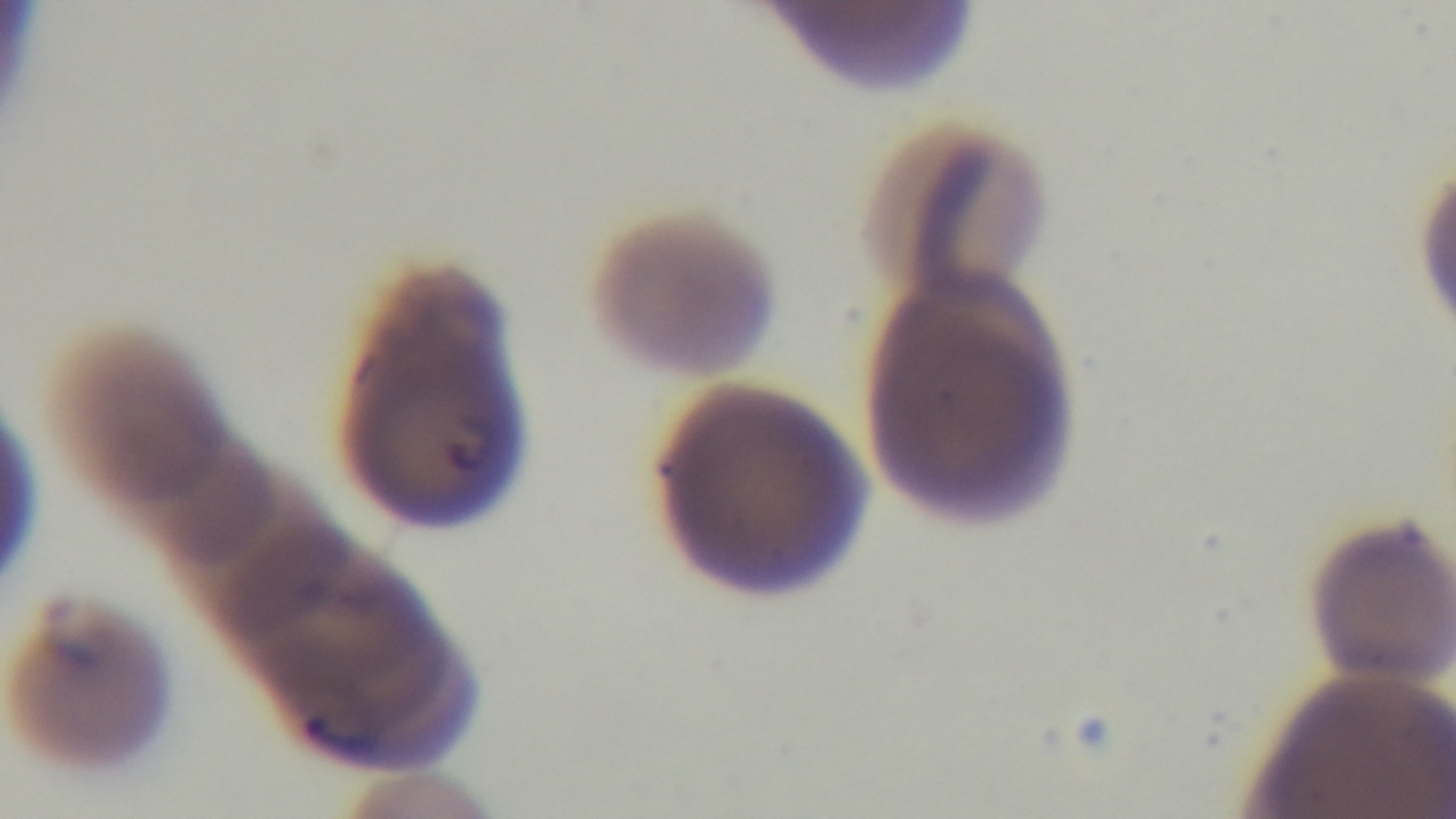
Summary:
  - Field of view: single
  - Capture: mounted 4K digital camera
  - Malaria status: positive
  - Modality: light microscopy
  - Preparation: thin
  - Stain: Giemsa
  - Objective: 100x oil immersion